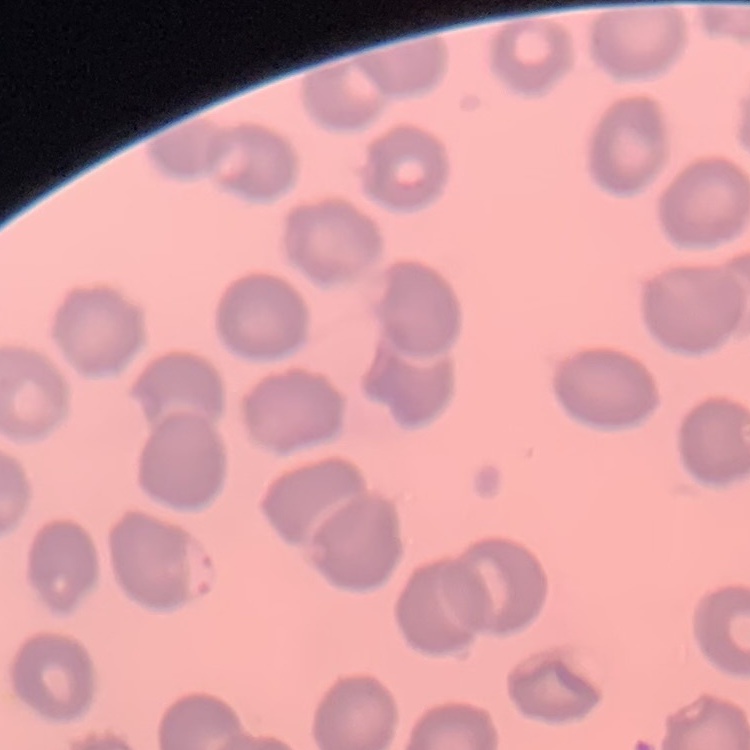

red_blood_cell_morphology: no rouleaux formation
preparation: thin peripheral smear
image_type: square crop of a larger photomicrograph
stain: Field's or Giemsa